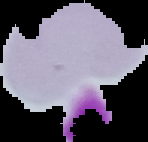
Summary:
  - Result: negative for malaria parasites
  - Image type: segmented cell region on a black background
  - Preparation: thin blood film
  - Image size: 148×142 pixels